Give a bounding box for every Plasmodium parasite, every leukocyte, and every artifact (stain precipitate or debris).
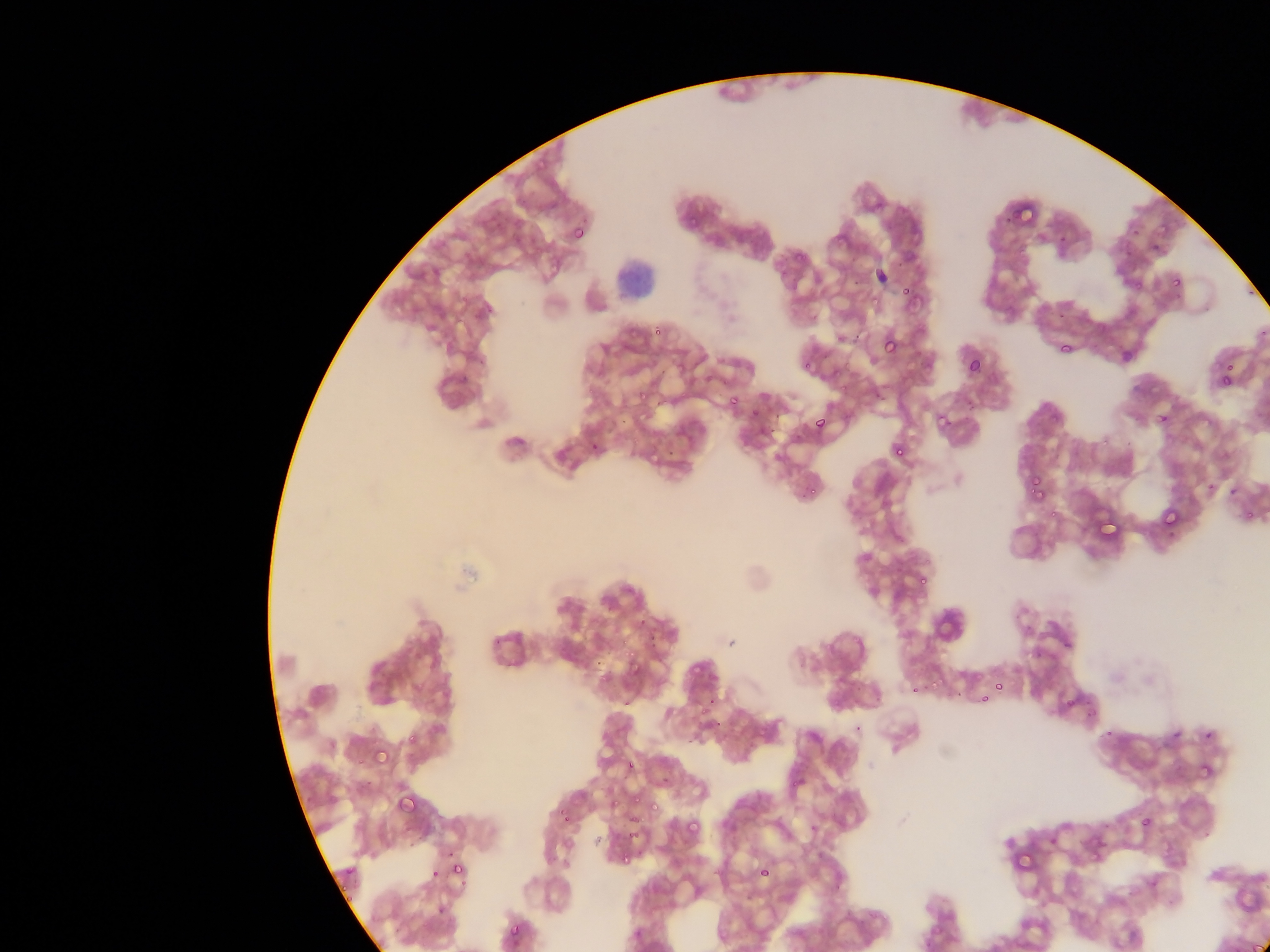

Approximate bounding boxes as [left, top, right, bottom] in pixels.
Plasmodium parasites: [686, 215, 700, 230], [572, 224, 588, 242], [895, 261, 905, 267], [1171, 276, 1183, 288], [901, 285, 913, 297], [810, 315, 817, 328], [653, 325, 665, 336], [854, 327, 861, 345], [882, 335, 899, 354], [1058, 339, 1075, 355], [798, 357, 816, 377], [965, 358, 981, 374], [1223, 361, 1235, 372], [1220, 364, 1234, 378], [657, 366, 668, 380], [1218, 374, 1234, 388], [834, 383, 853, 395], [730, 396, 740, 406], [874, 397, 890, 404], [653, 400, 662, 406], [749, 407, 760, 418], [1157, 412, 1170, 425], [774, 413, 782, 420], [941, 415, 952, 429], [814, 416, 827, 429], [765, 426, 778, 434], [589, 442, 600, 450], [894, 445, 907, 459], [665, 450, 673, 460], [1029, 475, 1043, 492], [806, 483, 824, 500], [1032, 484, 1047, 500], [1161, 507, 1179, 527], [916, 572, 931, 589], [639, 618, 647, 626], [646, 636, 659, 642], [1063, 639, 1074, 650], [648, 640, 656, 648], [929, 675, 938, 691], [910, 684, 920, 694], [996, 684, 1003, 693], [979, 695, 989, 704], [705, 698, 714, 709], [1065, 698, 1076, 708], [1103, 727, 1115, 738], [1204, 730, 1214, 740], [406, 731, 419, 746], [372, 746, 390, 765], [624, 758, 636, 771], [396, 793, 416, 812], [630, 794, 642, 807], [610, 799, 620, 809], [561, 812, 569, 823], [630, 814, 640, 824], [1141, 817, 1152, 827], [684, 818, 701, 836], [452, 861, 466, 876], [757, 865, 772, 879], [430, 868, 442, 881], [436, 904, 447, 915], [508, 921, 523, 940] | approximate [x, y] pixel centers of objects too small to bound: [854, 283].
Leukocytes: [599, 251, 670, 311].

capture = mobile-phone photograph through a microscope
country = Ghana
field of view = single
image size = 1270×952 pixels
preparation = thin blood smear